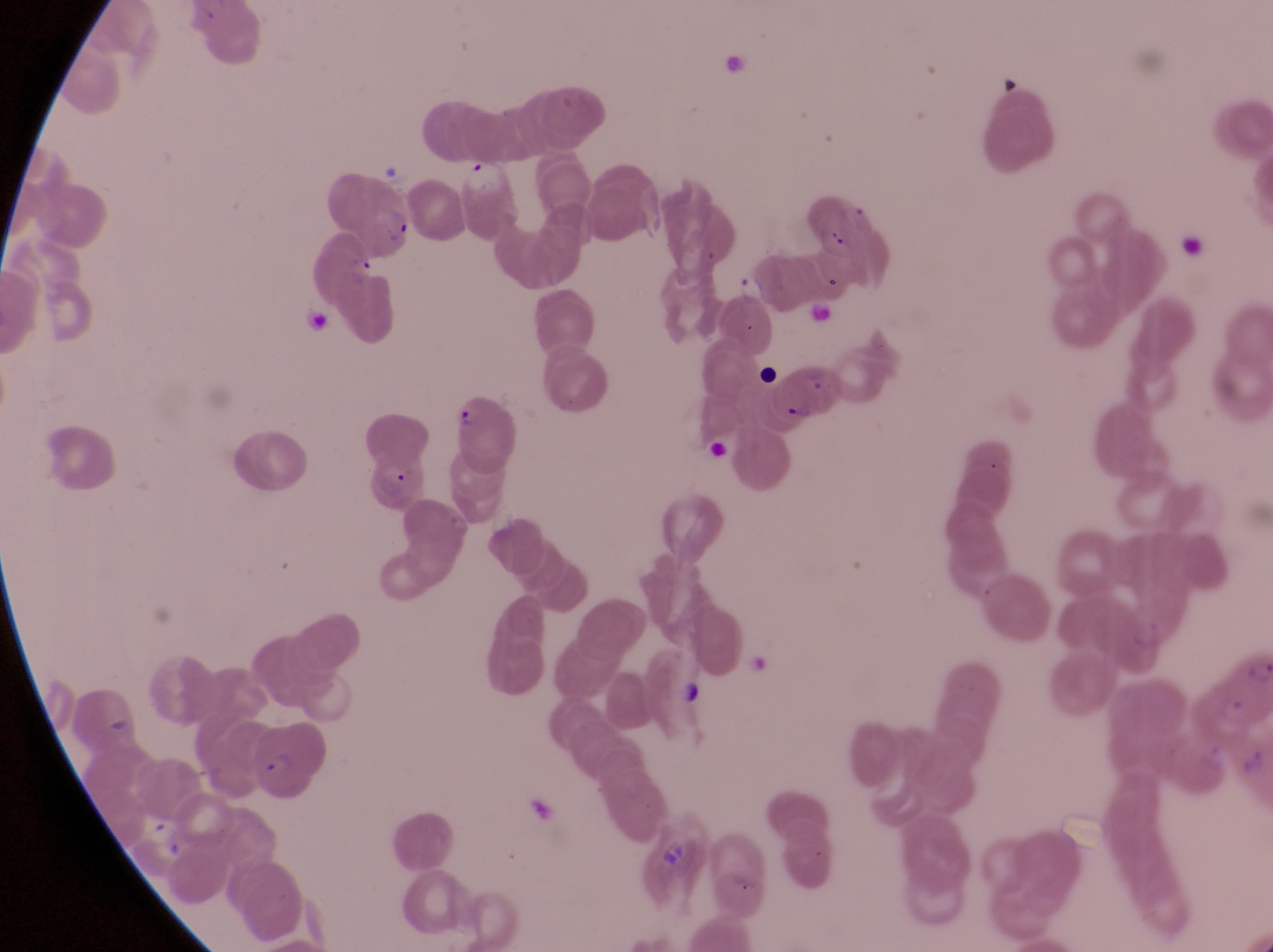

Approximate bounding boxes as left top right bottom in pixels.
Summary:
  - Artifact (platelet-like body, stain precipitate, or debris) locations: 819 220 851 255; 1174 234 1207 266; 749 362 777 387; 681 674 709 717; 652 836 692 876
  - Parasitised red blood cell locations: 766 365 841 430; 454 389 519 469; 245 727 335 795
  - Trophozoite locations: 349 257 379 285; 142 814 185 859
  - Country: Uganda
  - Capture: smartphone photograph through the eyepiece of an Olympus CX-23 microscope
  - Magnification: 1000x
  - Image size: 1273×952 pixels
  - Preparation: thin blood smear
  - Field of view: single